Report the malaria status of this cell.
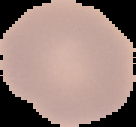
Uninfected.

From a thin blood film. Image is 136×127 pixels. The area outside the segmented cell region is set to black.